Outline each blood parasite and name the species.
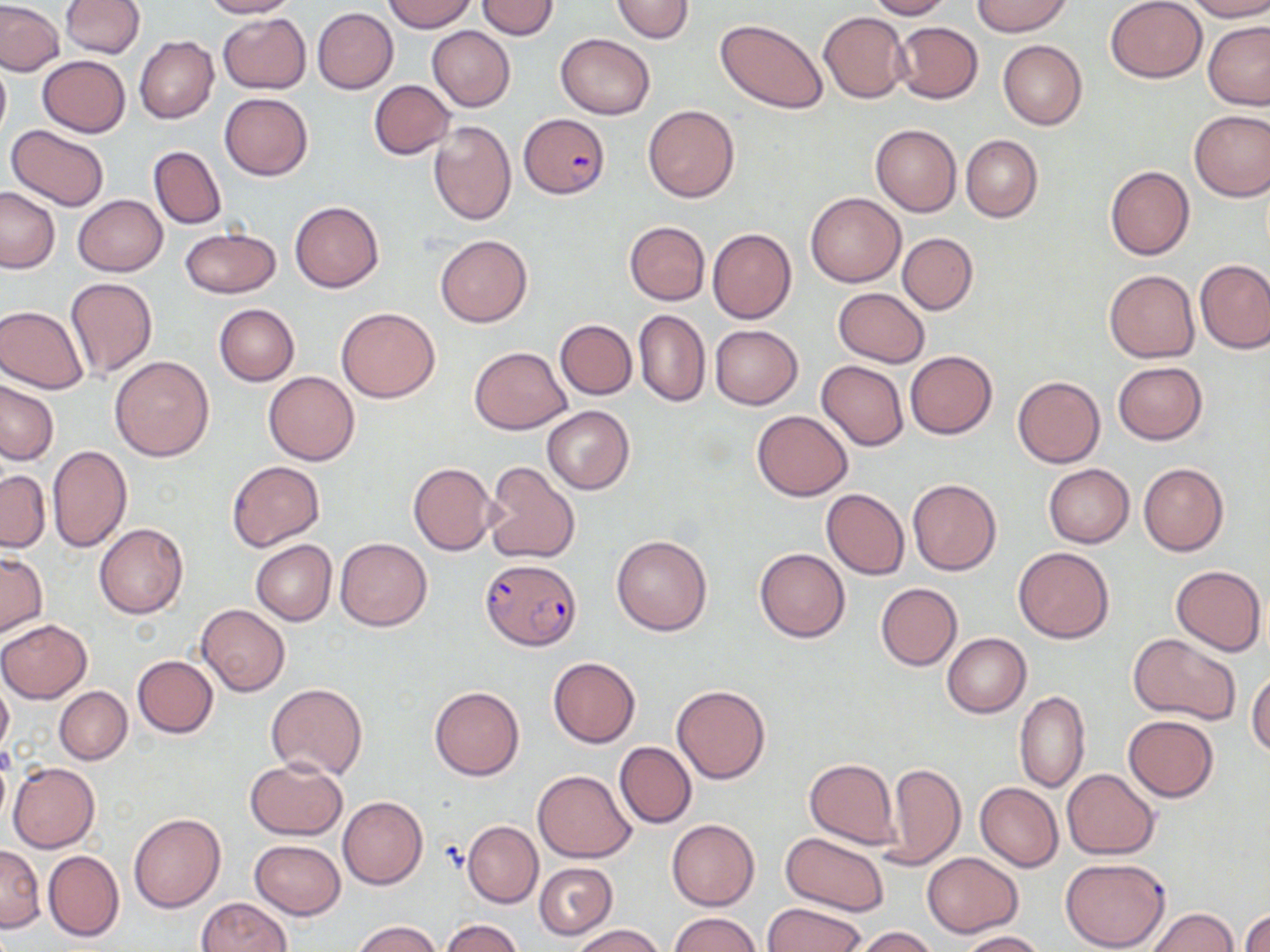

Approximate bounding boxes as [x1, y1, x2, y2] in pixels.
Plasmodium falciparum-infected red blood cells: [518, 113, 608, 197], [481, 558, 580, 649].
No Plasmodium ovale, Plasmodium malariae, Plasmodium vivax, Babesia divergens, or Trypanosoma brucei observed.

slide-level diagnosis = Plasmodium falciparum
modality = optical microscopy
uninfected red blood cell locations = approximate bounding boxes as [x1, y1, x2, y2] in pixels: [61, 0, 144, 57], [200, 0, 296, 18], [383, 0, 477, 32], [611, 0, 695, 44], [866, 0, 952, 19], [972, 0, 1071, 36], [1105, 0, 1207, 83], [1184, 0, 1270, 21], [0, 1, 65, 76], [476, 1, 559, 39], [312, 8, 398, 93], [818, 11, 910, 102], [218, 13, 311, 94], [715, 19, 827, 113], [893, 21, 983, 103], [1204, 23, 1270, 109], [427, 26, 515, 111], [557, 34, 655, 119], [134, 35, 219, 123], [998, 41, 1086, 129], [37, 55, 129, 137], [0, 56, 10, 142], [369, 80, 455, 160], [384, 86, 487, 193], [220, 92, 313, 181], [643, 105, 739, 202], [1188, 109, 1270, 201], [429, 120, 516, 225], [6, 124, 110, 212], [870, 124, 962, 216], [961, 134, 1042, 223], [147, 146, 226, 229], [1105, 165, 1194, 260], [0, 186, 60, 273], [806, 193, 904, 287], [73, 195, 168, 275], [290, 201, 384, 293], [624, 222, 710, 305], [707, 227, 797, 324], [179, 228, 281, 298], [897, 233, 978, 314], [435, 234, 532, 327], [1194, 259, 1270, 353], [1104, 269, 1200, 362], [65, 277, 157, 380], [834, 288, 929, 366], [215, 304, 299, 386], [0, 305, 90, 393], [336, 306, 441, 403], [634, 309, 710, 407], [555, 320, 637, 399], [710, 325, 803, 409], [469, 346, 571, 435], [906, 351, 996, 438], [110, 355, 215, 462], [816, 360, 909, 451], [1112, 362, 1208, 445], [264, 371, 360, 465], [1013, 376, 1105, 468], [1, 379, 59, 465], [542, 405, 635, 495], [752, 409, 853, 500], [47, 445, 132, 552], [227, 461, 323, 551], [484, 461, 580, 564], [408, 462, 496, 555], [1138, 462, 1228, 556], [1043, 464, 1134, 547], [0, 470, 49, 553], [908, 478, 1001, 576], [821, 489, 909, 579], [94, 523, 188, 618], [612, 534, 713, 635], [336, 538, 431, 630], [250, 539, 336, 625], [754, 547, 850, 642], [1013, 547, 1115, 643], [0, 552, 47, 636], [1170, 563, 1266, 656], [876, 583, 962, 670], [196, 604, 289, 695], [0, 620, 91, 702], [1129, 632, 1241, 724], [943, 633, 1031, 717], [132, 655, 219, 738], [548, 656, 641, 749], [1248, 668, 1270, 757], [0, 680, 13, 755], [266, 683, 367, 780], [672, 684, 771, 785], [430, 685, 524, 780], [54, 686, 131, 764], [1015, 690, 1089, 793], [1122, 715, 1219, 801], [614, 742, 697, 828], [244, 758, 348, 839], [804, 758, 898, 848], [8, 762, 98, 852], [885, 762, 965, 868], [1063, 769, 1158, 858], [532, 770, 635, 862], [975, 782, 1063, 873], [338, 796, 427, 889], [129, 813, 226, 912], [666, 818, 760, 910], [462, 820, 543, 908], [780, 831, 889, 915], [250, 839, 345, 920], [0, 844, 44, 931], [44, 850, 124, 941], [922, 852, 1024, 937], [1059, 858, 1170, 951], [534, 862, 617, 939], [196, 897, 291, 952], [763, 903, 866, 952], [1145, 908, 1238, 952], [1241, 910, 1269, 952], [669, 912, 761, 952], [439, 918, 523, 952], [354, 921, 439, 952], [570, 924, 662, 952], [849, 926, 940, 952], [960, 930, 1046, 951]
preparation = thin blood film
image size = 1270×952 pixels
magnification = 1000x
stain = May-Grünwald-Giemsa
field of view = one of a larger specimen